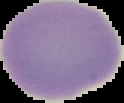

image size = 124×103 pixels
image type = segmented cell region on a black background
result = no malaria parasites seen
preparation = thin blood film